Point out each Plasmodium parasite.
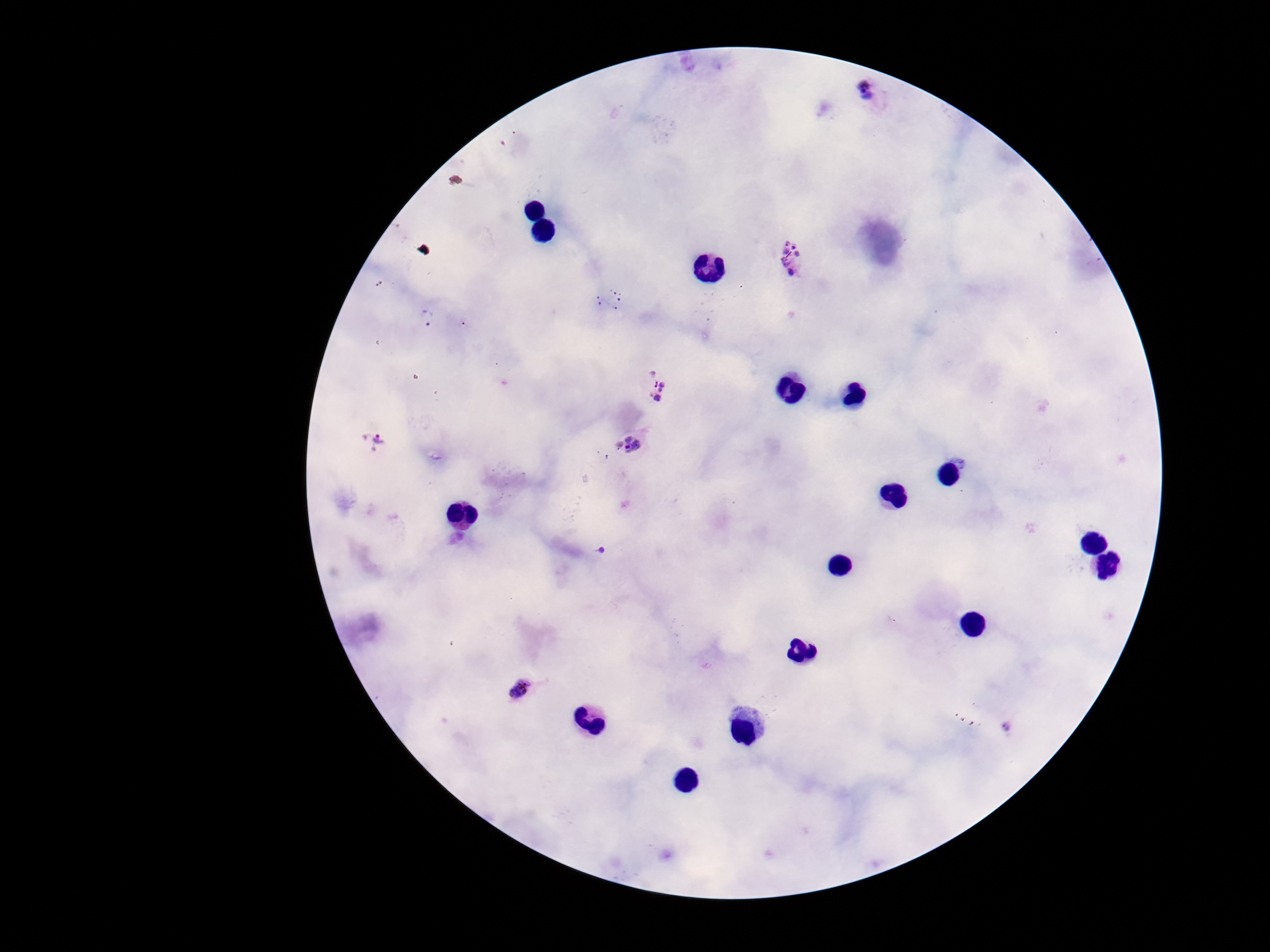

Approximate centers as (x, y) in pixels.
Plasmodium parasites: (872, 93), (793, 259), (427, 317), (657, 385), (374, 439), (629, 445), (520, 688).

patient malaria status = positive
field of view = one from this slide
preparation = thick peripheral-blood smear
stain = Giemsa
image size = 1270×952 pixels
capture = smartphone camera through the microscope eyepiece
magnification = 100x